Give the extent of all Plasmodium ovale-infected red blood cells.
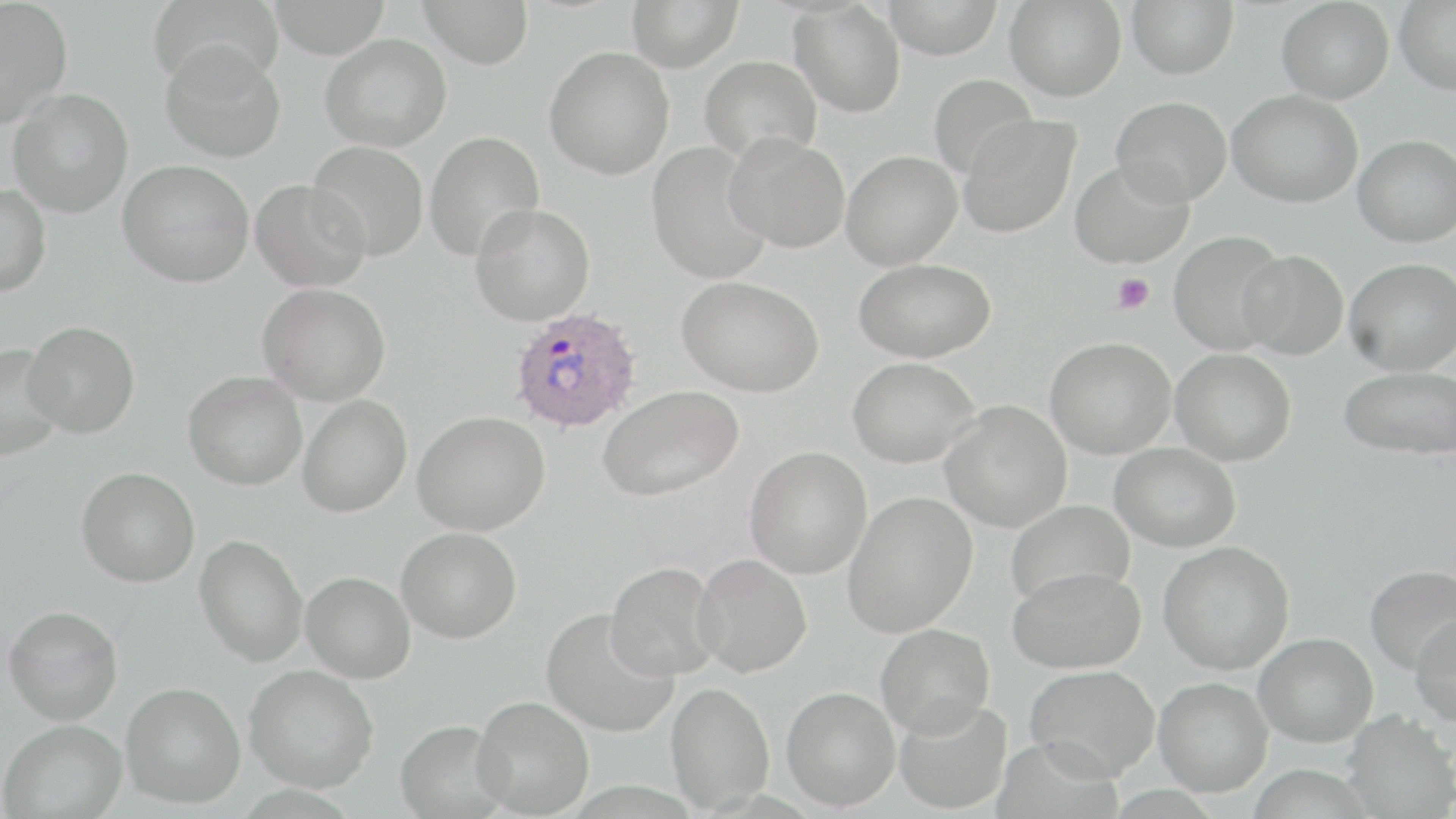

Approximate bounding boxes as named x1/y1/x2/y2 corners in pixels.
Plasmodium ovale-infected red blood cells: (x1=508, y1=307, x2=643, y2=433).

Summary:
  - Uninfected red blood cell locations: (x1=0, y1=0, x2=73, y2=126), (x1=147, y1=0, x2=283, y2=90), (x1=267, y1=0, x2=392, y2=58), (x1=419, y1=0, x2=534, y2=68), (x1=626, y1=0, x2=743, y2=72), (x1=883, y1=0, x2=1003, y2=58), (x1=1005, y1=0, x2=1127, y2=101), (x1=1127, y1=0, x2=1238, y2=79), (x1=1394, y1=0, x2=1456, y2=95), (x1=789, y1=1, x2=906, y2=117), (x1=1277, y1=1, x2=1394, y2=104), (x1=320, y1=33, x2=452, y2=151), (x1=160, y1=41, x2=286, y2=162), (x1=544, y1=46, x2=675, y2=179), (x1=699, y1=55, x2=822, y2=164), (x1=929, y1=73, x2=1038, y2=181), (x1=8, y1=88, x2=133, y2=218), (x1=1228, y1=89, x2=1363, y2=207), (x1=1111, y1=96, x2=1232, y2=207), (x1=957, y1=114, x2=1081, y2=238), (x1=424, y1=131, x2=545, y2=262), (x1=724, y1=133, x2=850, y2=253), (x1=1354, y1=134, x2=1456, y2=247), (x1=308, y1=140, x2=429, y2=261), (x1=647, y1=141, x2=774, y2=284), (x1=841, y1=151, x2=962, y2=270), (x1=118, y1=159, x2=255, y2=286), (x1=1070, y1=159, x2=1194, y2=268), (x1=251, y1=179, x2=371, y2=292), (x1=0, y1=183, x2=51, y2=296), (x1=470, y1=204, x2=595, y2=325), (x1=1169, y1=231, x2=1288, y2=355), (x1=1237, y1=249, x2=1348, y2=360), (x1=854, y1=258, x2=996, y2=362), (x1=1345, y1=258, x2=1456, y2=375), (x1=677, y1=276, x2=825, y2=397), (x1=257, y1=283, x2=390, y2=405), (x1=23, y1=320, x2=140, y2=439), (x1=1045, y1=337, x2=1175, y2=458), (x1=0, y1=343, x2=64, y2=460), (x1=1171, y1=348, x2=1296, y2=466), (x1=847, y1=357, x2=981, y2=468), (x1=1339, y1=365, x2=1456, y2=460), (x1=183, y1=371, x2=307, y2=490), (x1=598, y1=384, x2=743, y2=500), (x1=298, y1=395, x2=412, y2=517), (x1=940, y1=400, x2=1071, y2=532), (x1=413, y1=411, x2=550, y2=535), (x1=1111, y1=442, x2=1241, y2=552), (x1=745, y1=446, x2=872, y2=579), (x1=77, y1=467, x2=200, y2=587), (x1=843, y1=491, x2=977, y2=637), (x1=1005, y1=499, x2=1135, y2=608), (x1=397, y1=527, x2=521, y2=643), (x1=194, y1=534, x2=308, y2=666), (x1=1159, y1=540, x2=1295, y2=674), (x1=692, y1=554, x2=812, y2=677), (x1=605, y1=562, x2=724, y2=682), (x1=1365, y1=565, x2=1456, y2=674), (x1=1009, y1=566, x2=1146, y2=673), (x1=301, y1=571, x2=415, y2=683), (x1=3, y1=605, x2=123, y2=724), (x1=541, y1=608, x2=677, y2=737), (x1=1410, y1=614, x2=1456, y2=727), (x1=876, y1=623, x2=995, y2=739), (x1=1254, y1=632, x2=1377, y2=747), (x1=244, y1=664, x2=379, y2=792), (x1=1025, y1=664, x2=1159, y2=781), (x1=1154, y1=676, x2=1273, y2=797), (x1=666, y1=681, x2=774, y2=812), (x1=120, y1=682, x2=245, y2=808), (x1=782, y1=686, x2=901, y2=810), (x1=471, y1=695, x2=594, y2=817), (x1=893, y1=696, x2=1012, y2=814), (x1=1341, y1=710, x2=1456, y2=818), (x1=0, y1=718, x2=127, y2=818), (x1=394, y1=719, x2=510, y2=818)
  - Platelet locations: (x1=1111, y1=273, x2=1154, y2=314)
  - Slide-level diagnosis: Plasmodium ovale
  - Stain: May-Grünwald-Giemsa
  - Modality: light microscopy
  - Field of view: single
  - Image size: 1456×819 pixels
  - Preparation: thin blood smear
  - Magnification: 1000x